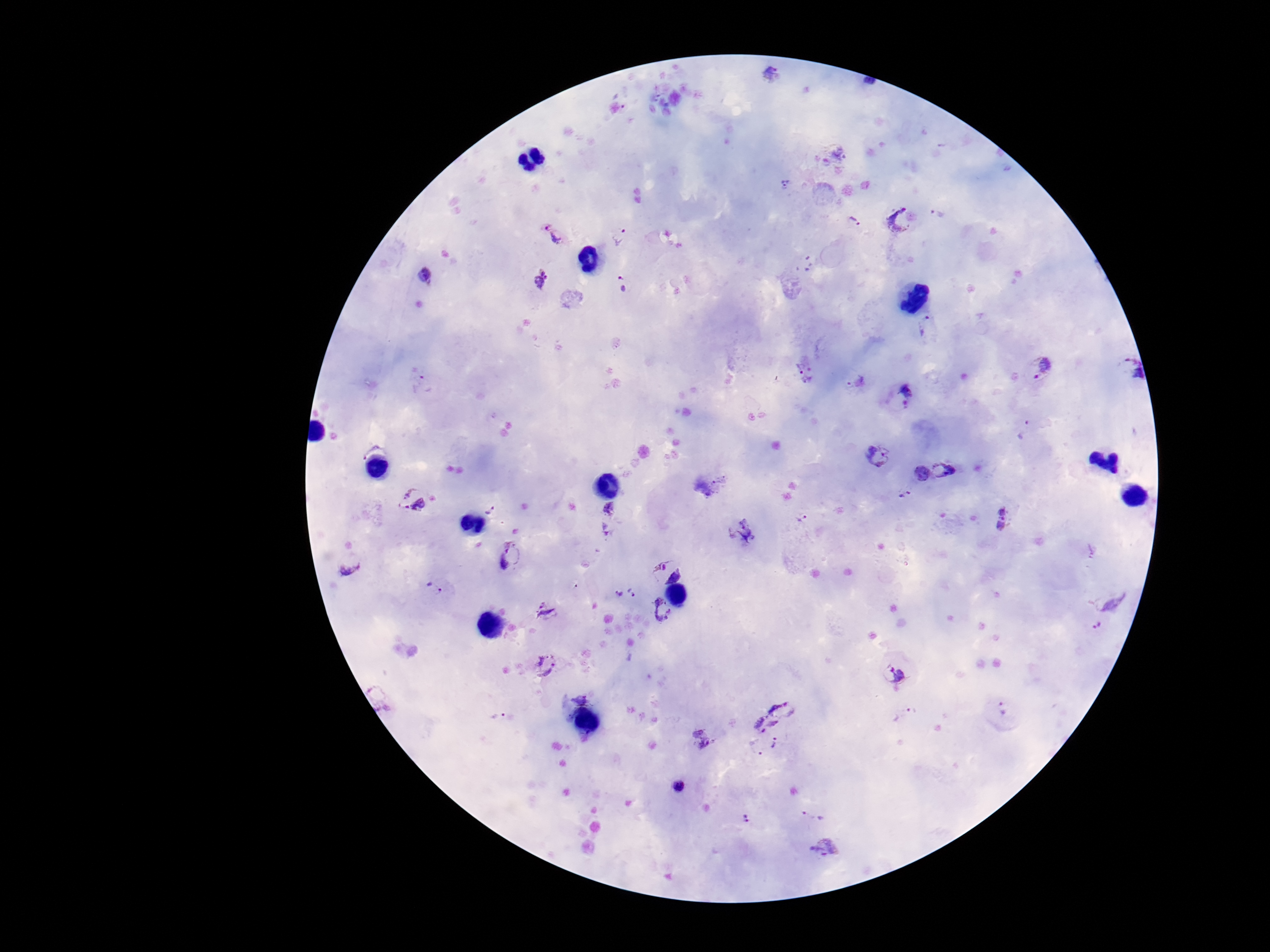

Approximate centers as [x, y] in pixels.
Summary:
  - Plasmodium parasite locations: [770, 73], [786, 184], [937, 212], [901, 219], [854, 223], [550, 234], [621, 235], [426, 275], [541, 278], [624, 284], [920, 326], [1041, 367], [801, 368], [1125, 370], [856, 383], [426, 384], [906, 391], [1024, 429], [878, 456], [945, 470], [918, 471], [906, 494], [412, 498], [494, 510], [802, 518], [1004, 519], [512, 557], [349, 569], [667, 571], [435, 589], [633, 592], [617, 594], [1112, 599], [661, 610], [547, 614], [1099, 626], [545, 665], [893, 673], [581, 698], [785, 707], [1004, 708], [902, 713], [499, 717], [760, 725], [700, 738], [775, 741], [751, 749], [680, 787], [814, 816], [746, 818], [826, 846]
  - Image size: 1270×952 pixels
  - Preparation: thick blood smear
  - Stain: Giemsa
  - Magnification: 100x
  - Field of view: one from this slide
  - Patient malaria status: infected
  - Capture: smartphone camera through the microscope eyepiece